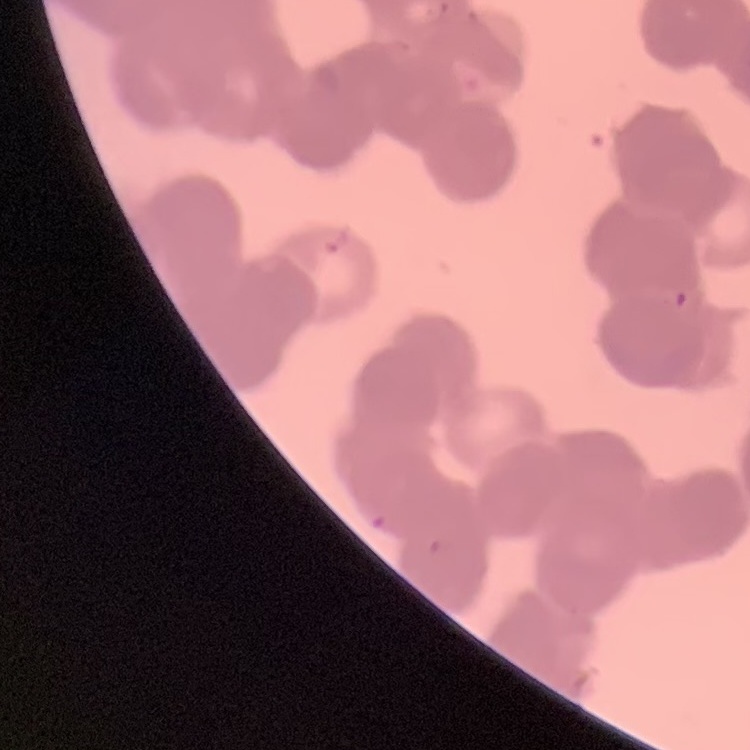
{
  "red_blood_cell_morphology": "rouleaux formation",
  "preparation": "thin peripheral smear",
  "image_type": "one tile cut from a larger photomicrograph",
  "stain": "Field's or Giemsa"
}